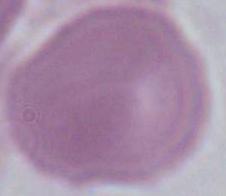
Captured at 1000x magnification. Photomicrograph. A red blood cell is seen.